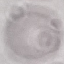
Summary:
  - Malaria status: uninfected
  - Image type: automatically extracted cell patch, resized to 64 × 64 pixels
  - Capture: smartphone camera at the microscope eyepiece
  - Stain: Giemsa
  - Preparation: thin blood smear